Describe the morphology of the red blood cells.
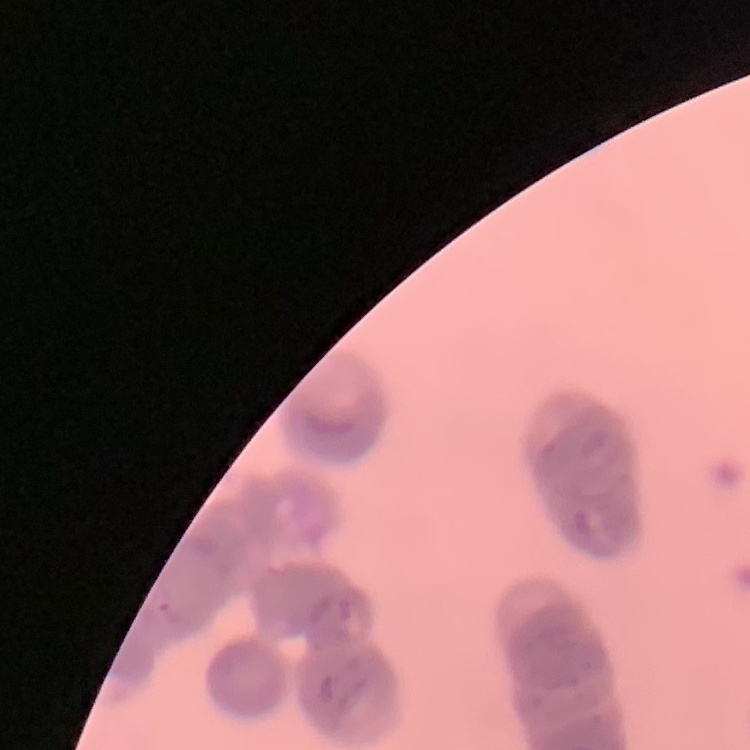
They show rouleaux formation.

preparation = thin blood film
stain = Field's or Giemsa
image type = square crop of a larger photomicrograph